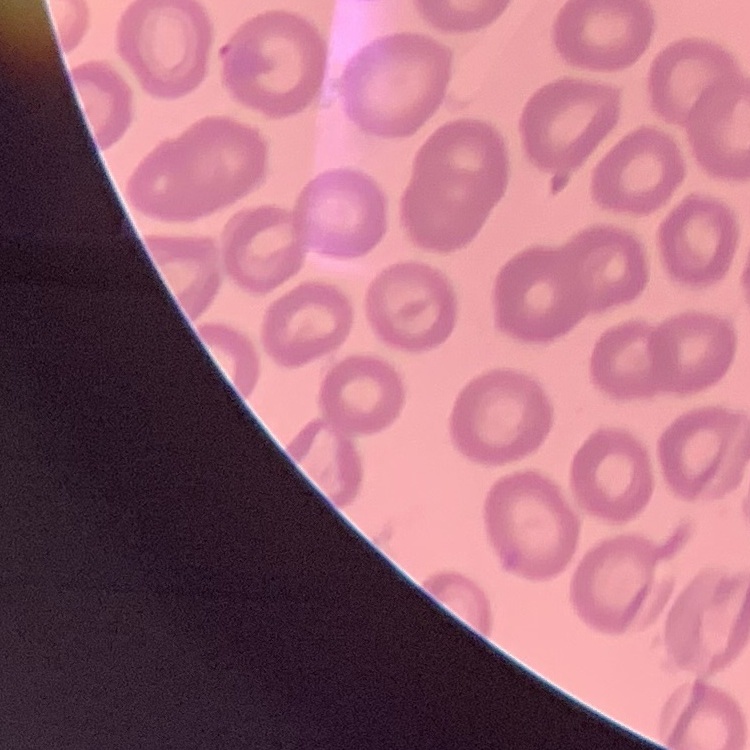
red blood cell morphology = no rouleaux formation
preparation = thin blood smear
image type = square crop of a larger photomicrograph
stain = Field's or Giemsa